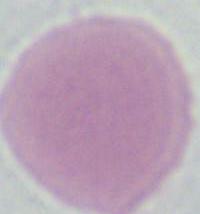

Summary:
  - Identification: erythrocyte
  - Modality: photomicrograph
  - Magnification: 1000x